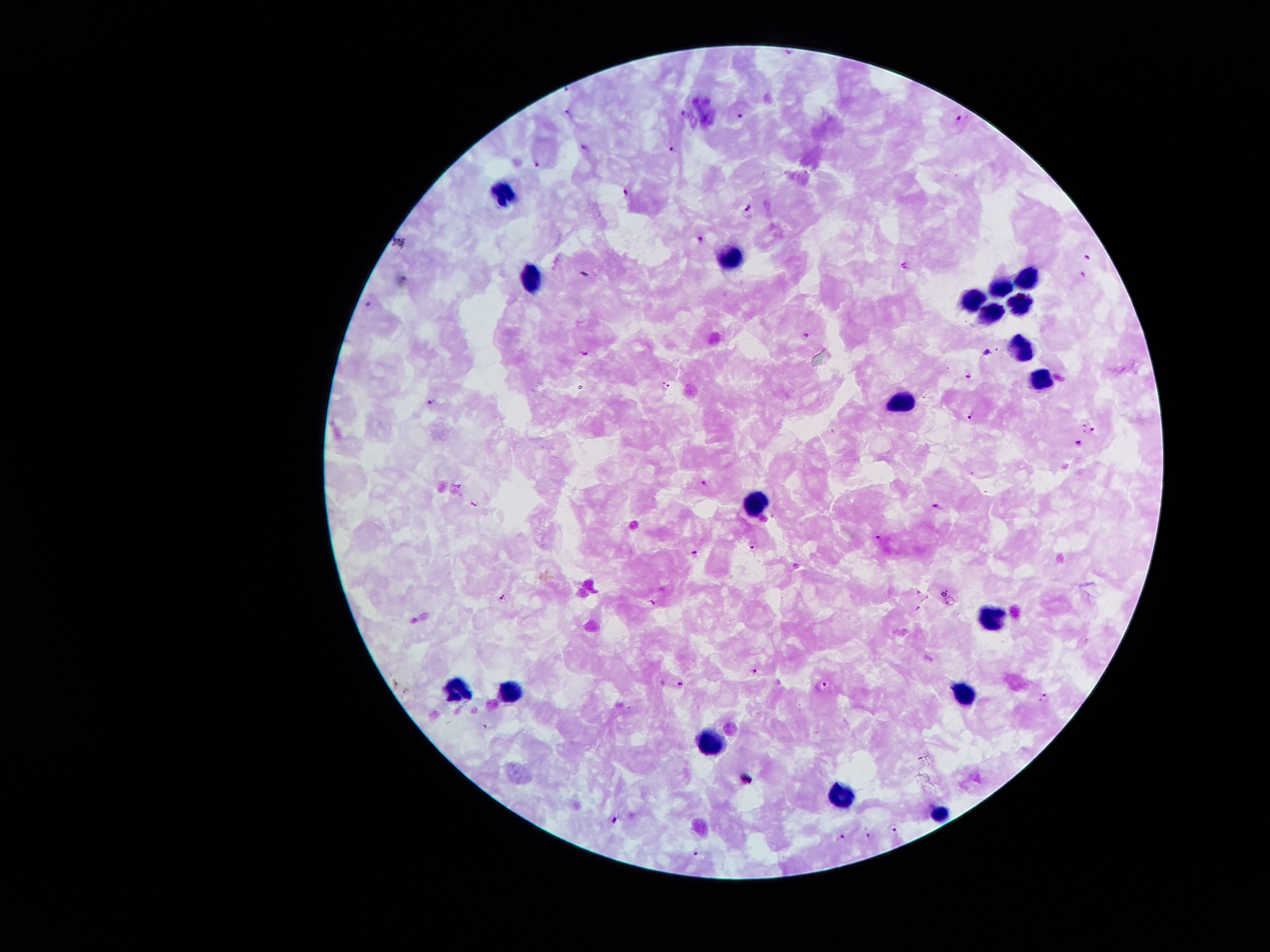

coordinate format = approximate object centers, in pixels from the top-left corner
leukocyte locations = (x=503, y=193), (x=729, y=256), (x=1027, y=277), (x=530, y=279), (x=999, y=287), (x=973, y=296), (x=1020, y=303), (x=990, y=313), (x=1021, y=344), (x=1040, y=381), (x=899, y=400), (x=757, y=504), (x=994, y=612), (x=456, y=688), (x=967, y=693), (x=508, y=694), (x=711, y=744), (x=841, y=796), (x=943, y=811)
Plasmodium parasite locations = (x=566, y=87), (x=568, y=111), (x=683, y=115), (x=740, y=117), (x=960, y=118), (x=585, y=147), (x=671, y=150), (x=537, y=164), (x=628, y=191), (x=747, y=209), (x=701, y=240), (x=1088, y=258), (x=905, y=266), (x=586, y=273), (x=1083, y=275), (x=368, y=305), (x=807, y=336), (x=988, y=350), (x=584, y=353), (x=969, y=375), (x=667, y=386), (x=431, y=403), (x=970, y=415), (x=1085, y=427), (x=1093, y=429), (x=1079, y=443), (x=703, y=483), (x=459, y=485), (x=475, y=504), (x=938, y=505), (x=879, y=538), (x=752, y=546), (x=695, y=551), (x=503, y=597), (x=651, y=601), (x=919, y=608), (x=754, y=670), (x=680, y=684), (x=824, y=684), (x=1043, y=698), (x=615, y=821), (x=895, y=828), (x=868, y=836), (x=840, y=838), (x=694, y=851)
magnification = 100x
patient malaria status = positive for Plasmodium falciparum
image size = 1270×952 pixels
stain = Giemsa
preparation = thick peripheral-blood smear
capture = smartphone through the microscope eyepiece
field of view = one from this slide